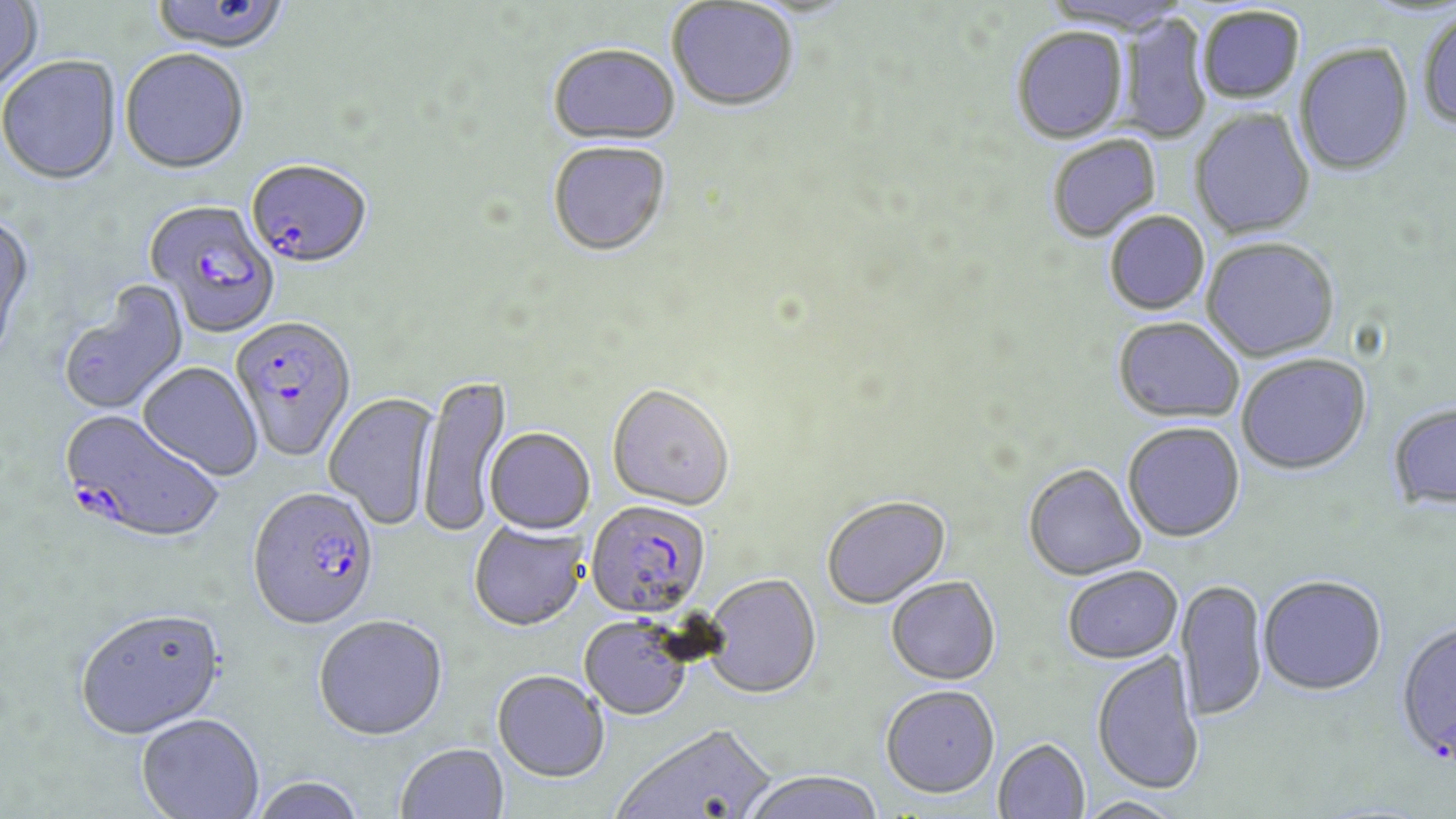

Summary:
  - Coordinate format: approximate bounding boxes as (x1, y1, x2, y2) in pixels
  - Plasmodium falciparum-infected red blood cell locations: (246, 162, 373, 271), (145, 200, 280, 339), (230, 316, 358, 464), (62, 411, 223, 548), (247, 490, 380, 633), (585, 501, 710, 620)
  - Uninfected red blood cell locations: (0, 0, 43, 99), (150, 0, 291, 58), (666, 2, 798, 113), (1197, 7, 1304, 104), (1418, 10, 1456, 132), (1121, 13, 1212, 144), (1011, 28, 1129, 145), (1295, 44, 1414, 176), (547, 46, 681, 149), (119, 51, 249, 177), (0, 57, 122, 188), (1190, 109, 1315, 240), (1047, 136, 1161, 244), (548, 144, 671, 260), (1104, 211, 1210, 316), (0, 212, 38, 369), (1202, 239, 1339, 363), (57, 280, 190, 416), (1112, 318, 1245, 423), (1236, 354, 1371, 475), (137, 363, 263, 482), (417, 375, 513, 538), (607, 386, 735, 513), (324, 393, 440, 532), (1387, 402, 1456, 513), (1123, 422, 1245, 542), (484, 428, 595, 536), (1023, 464, 1146, 581), (821, 495, 951, 609), (468, 521, 588, 633), (1062, 566, 1183, 664), (703, 574, 821, 699), (1257, 575, 1387, 695), (886, 577, 1000, 685), (1175, 578, 1267, 722), (74, 609, 227, 740), (313, 617, 448, 743), (579, 617, 692, 720), (1395, 618, 1456, 765), (1091, 652, 1205, 795), (492, 671, 609, 783), (879, 685, 1000, 799), (136, 715, 265, 819), (611, 724, 775, 819), (994, 739, 1090, 818), (396, 744, 509, 819), (741, 769, 884, 819), (249, 777, 368, 819), (1076, 796, 1185, 819)
  - Slide-level diagnosis: Plasmodium falciparum
  - Field of view: one of a larger specimen
  - Image size: 1456×819 pixels
  - Modality: optical microscopy
  - Magnification: 1000x
  - Preparation: thin blood film
  - Stain: May-Grünwald-Giemsa